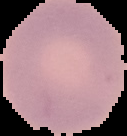

{
  "image_size": "127×136 pixels",
  "malaria_status": "uninfected",
  "image_type": "segmented cell region with the area outside set to black",
  "preparation": "thin blood film"
}